Point out each Plasmodium parasite.
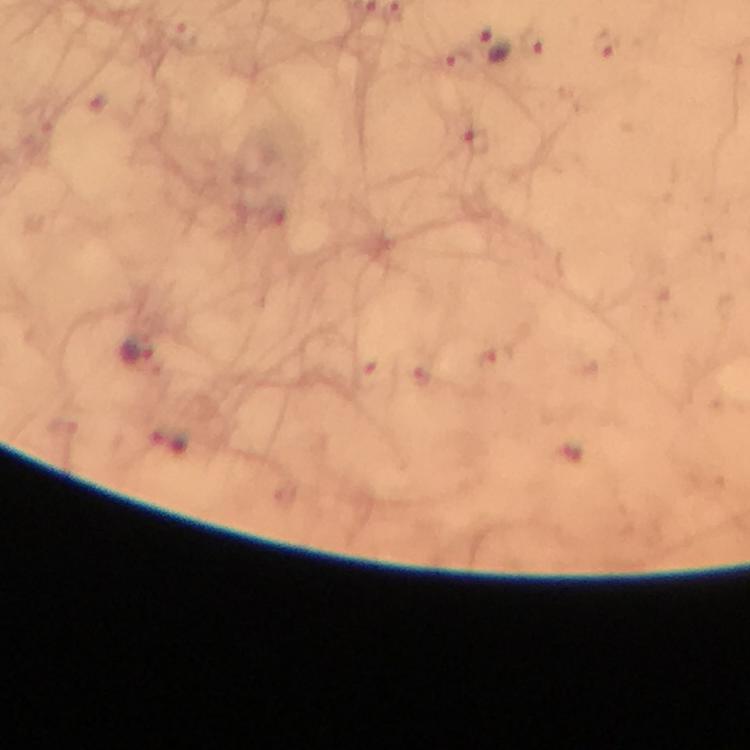
Approximate centers as [x, y] in pixels.
Plasmodium parasites: [496, 44], [604, 44], [136, 351], [169, 440].

cropped from = one field of view
immersion oil = applied
capture = smartphone photograph through a microscope
stain = Giemsa
preparation = thick blood smear
image size = 750×750 pixels
context = from a diagnostic examination for malaria
magnification = 100x